Classify this cell by malaria status.
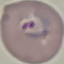
It is parasitized.

capture: smartphone camera at the microscope eyepiece
stain: Giemsa
image_type: automatically extracted cell patch, resized to 64 × 64 pixels
preparation: thin smear